Report the malaria status of this cell.
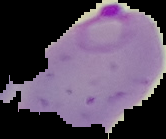

Parasitized.

Summary:
  - Image size: 166×139 pixels
  - Preparation: thin blood smear
  - Image type: segmented cell region with the area outside set to black